Identify the malaria species.
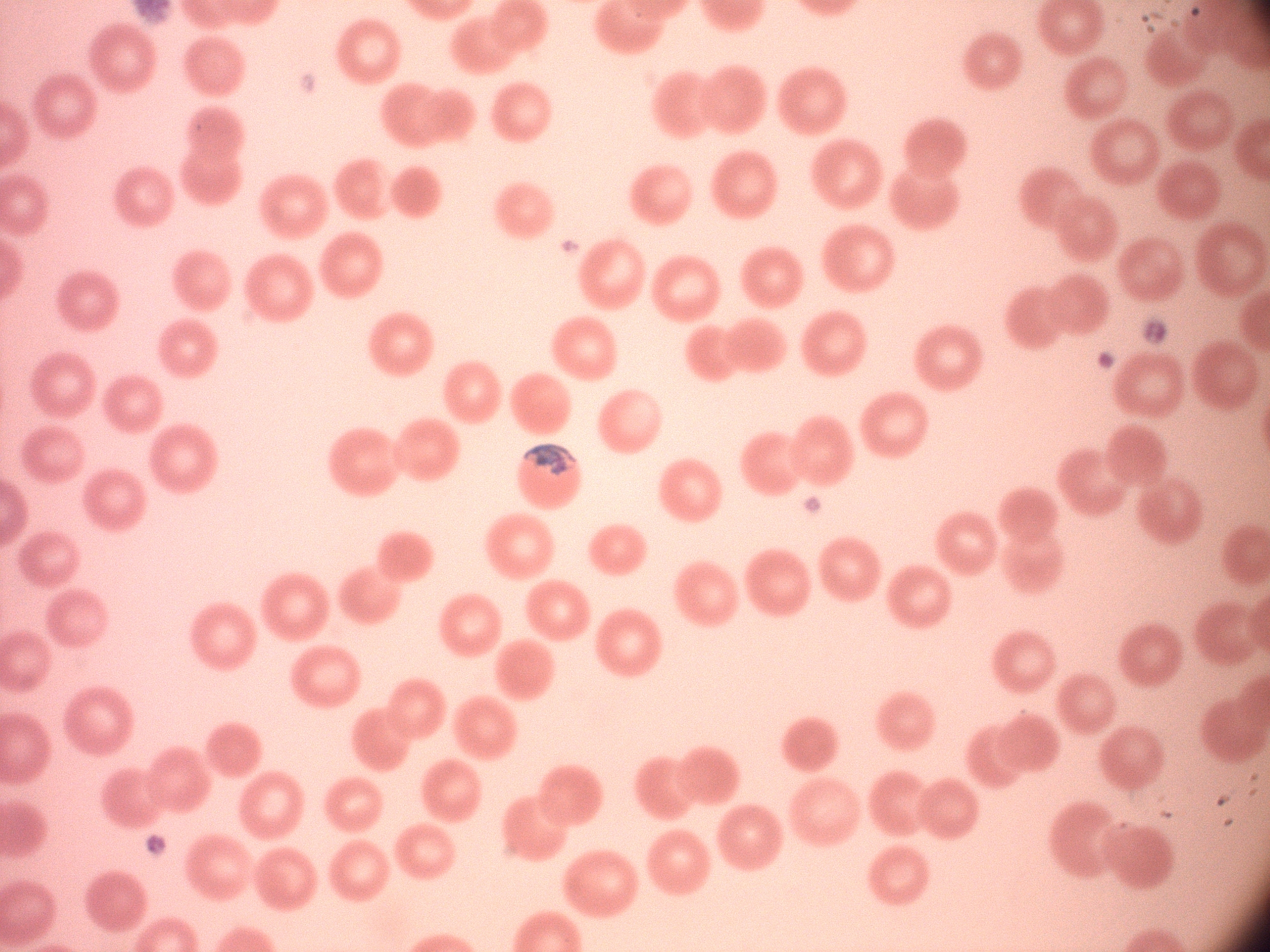

Plasmodium malariae.

Approximate bounding boxes as (x1, y1, x2, y2) in pixels, from the source annotation, which is not necessarily exhaustive. Trophozoite locations: (524, 443, 577, 476). Leica DM2000 optical microscope with a built-in camera. Thin blood film. 100x magnification. One field from this slide. Image is 1270×952 pixels. Giemsa-stained preparation.